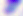

Micrograph. 400x magnification. Toxoplasma gondii is shown.